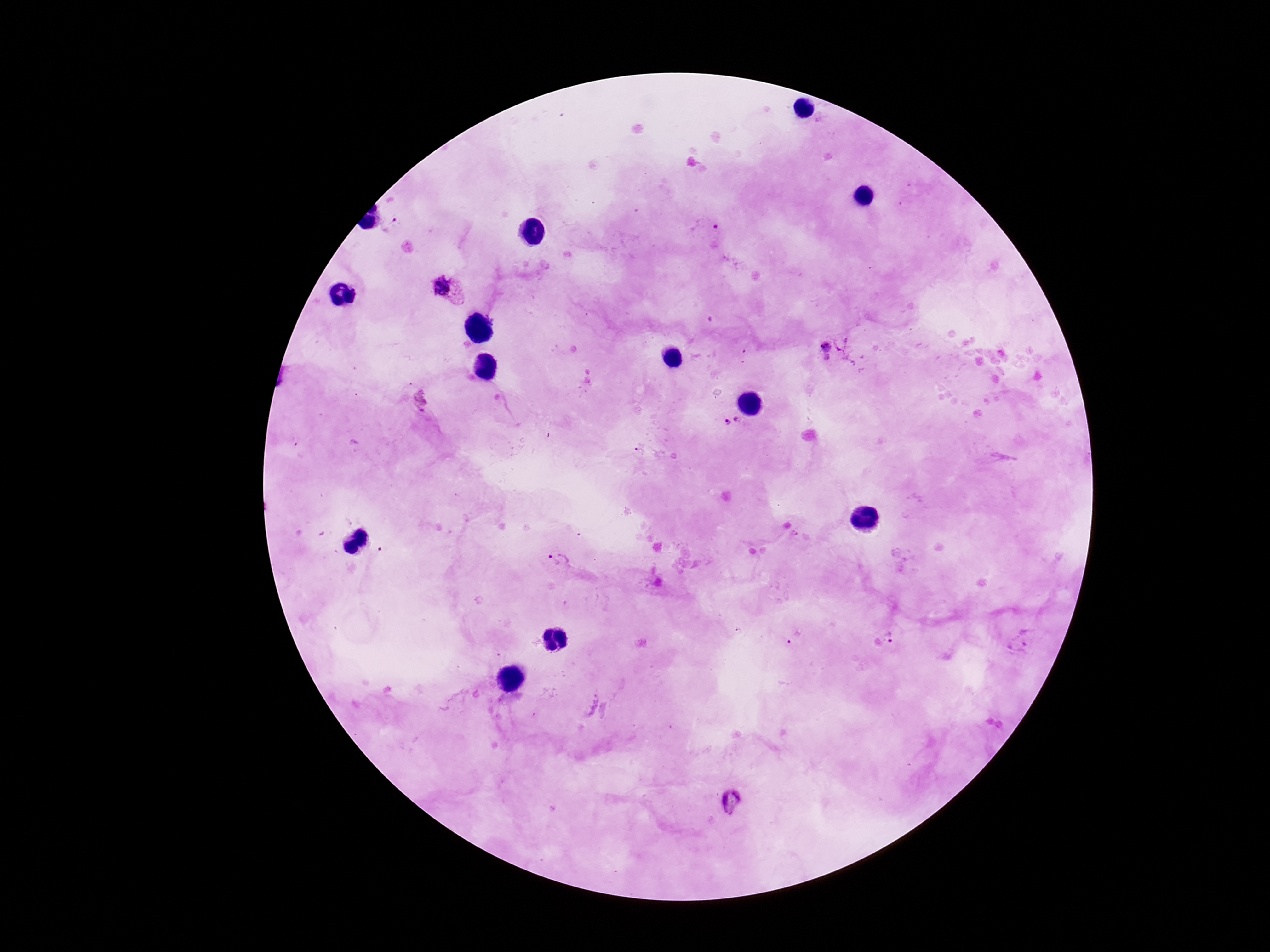
Approximate centers as [x, y] in pixels.
Summary:
  - Plasmodium parasite locations: [705, 227], [450, 291], [826, 345], [827, 359], [420, 400], [732, 421], [646, 453], [562, 563], [794, 636], [889, 636], [732, 802]
  - Preparation: thick peripheral-blood smear
  - Capture: smartphone camera through the microscope eyepiece
  - Stain: Giemsa
  - Image size: 1270×952 pixels
  - Field of view: one from this slide
  - Magnification: 100x
  - Patient malaria status: infected